Point out each leukocyte.
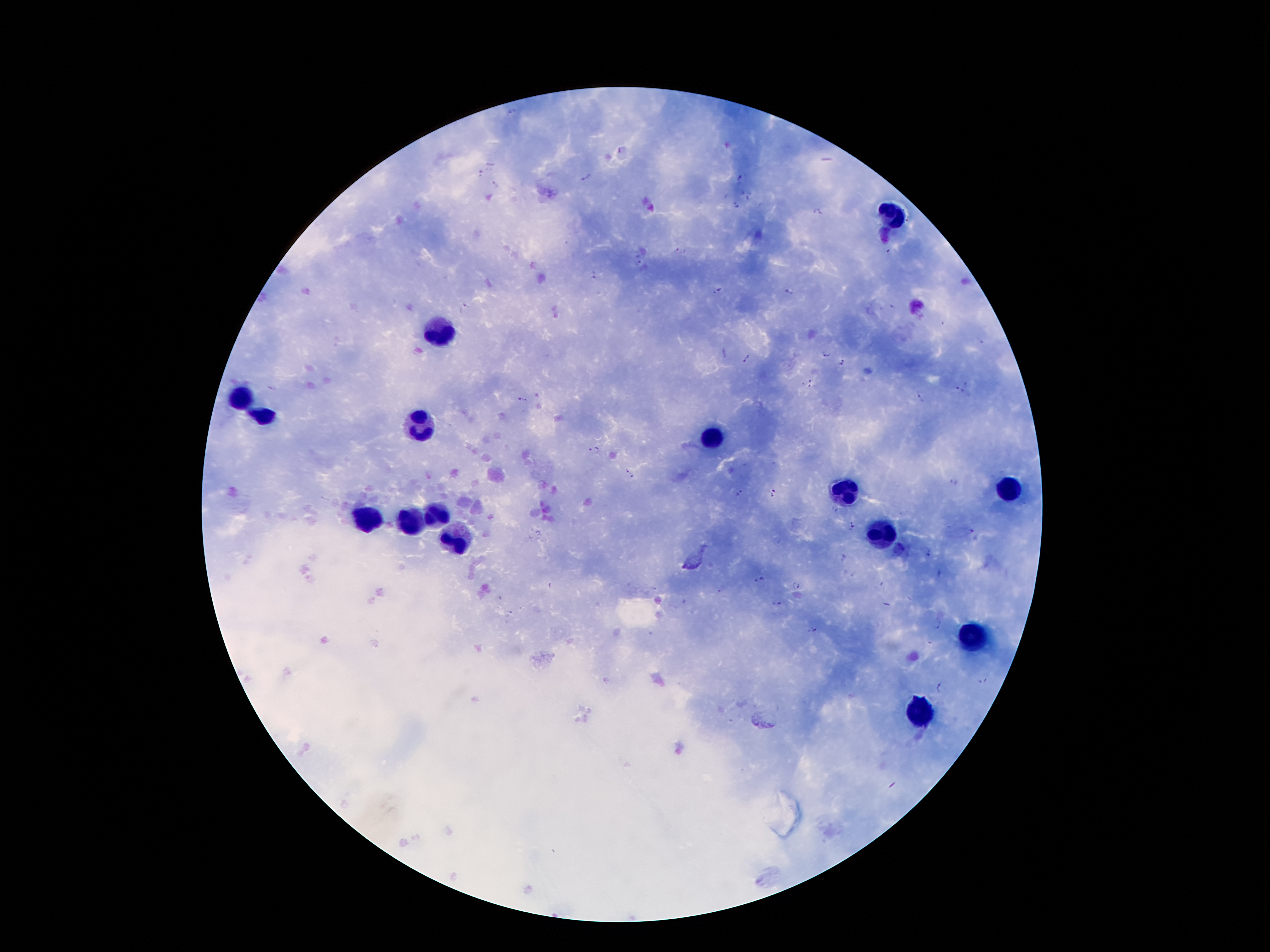
Approximate centers as {x, y} in pixels.
Leukocytes: {892, 217}, {437, 328}, {242, 399}, {264, 417}, {420, 422}, {712, 436}, {1013, 486}, {848, 491}, {437, 518}, {363, 523}, {410, 523}, {887, 535}, {455, 540}, {974, 634}, {919, 711}.

field_of_view: one from this slide
image_size: 1270×952 pixels
plasmodium_parasite_locations: 'approximate centers as {x, y} in pixels: {511, 112}, {622, 149}, {490, 165}, {481, 174}, {586, 177}, {737, 177}, {494, 183}, {747, 193}, {736, 205}, {817, 212}, {680, 250}, {885, 250}, {638, 259}, {593, 274}, {720, 290}, {791, 291}, {464, 307}, {826, 353}, {748, 358}, {842, 362}, {807, 384}, {967, 385}, {273, 389}, {958, 391}, {918, 397}, {523, 400}, {595, 449}, {632, 474}, {954, 482}, {740, 493}, {771, 494}, {833, 509}, {853, 526}, {969, 530}, {927, 554}, {844, 557}, {939, 574}, {760, 581}, {796, 586}, {720, 590}, {777, 604}, {509, 614}, {937, 625}, {812, 630}, {982, 682}, {938, 688}'
magnification: 100x
capture: smartphone through the microscope eyepiece
preparation: thick blood smear
stain: Giemsa
patient_malaria_status: positive for Plasmodium falciparum